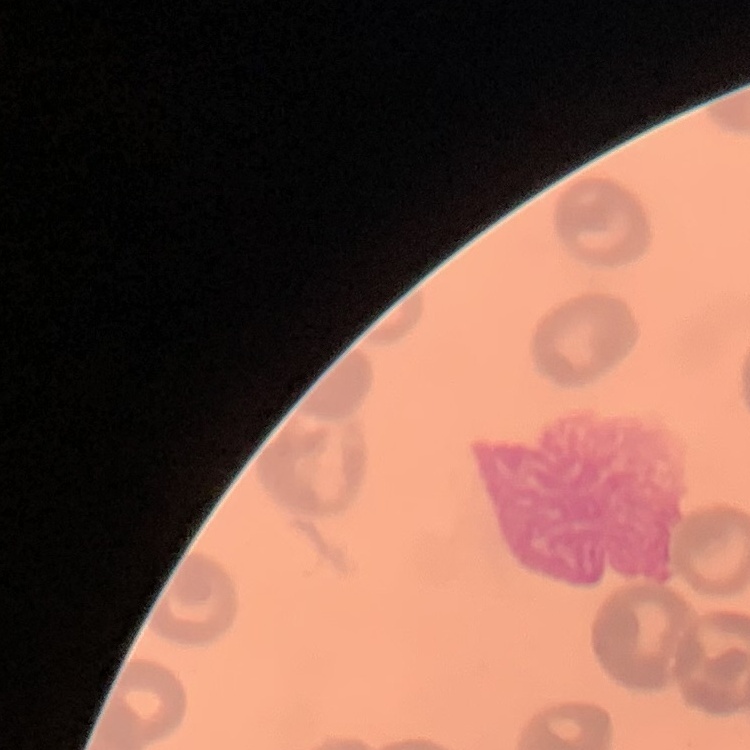

The red blood cells exhibit no rouleaux formation. Thin blood smear. Stained with either Field's or Giemsa. Square crop of a larger photomicrograph.